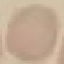
Summary:
  - Malaria status: uninfected
  - Image type: cell patch, automatically extracted from a larger field of view and resized to 64 × 64 pixels
  - Capture: smartphone camera at the microscope eyepiece
  - Stain: Giemsa
  - Preparation: thin smear